Give the extent of all uninfected red blood cells.
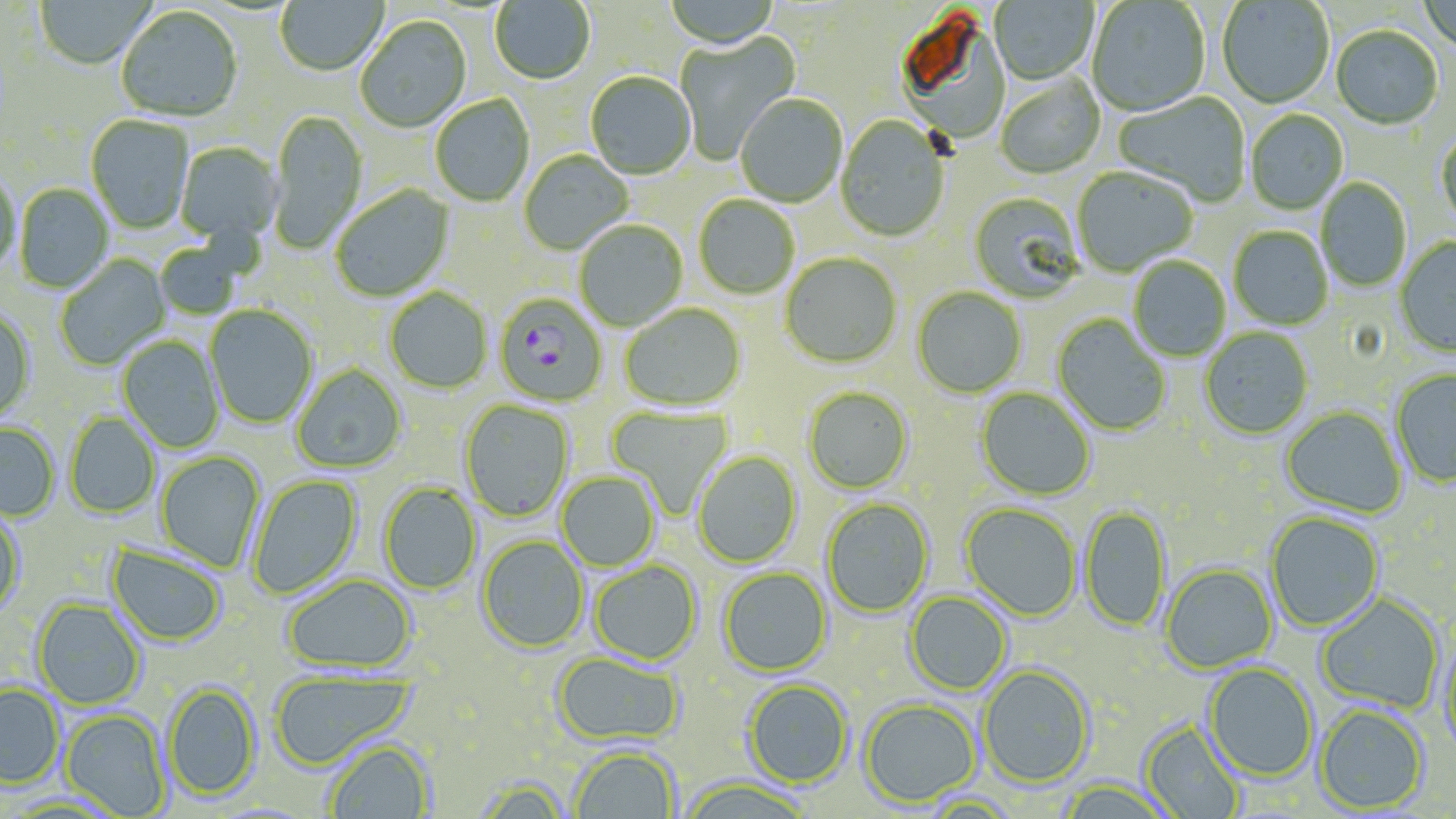
Approximate bounding boxes as (x1, y1, x2, y2) in pixels.
Uninfected red blood cells: (275, 0, 388, 78), (664, 0, 780, 51), (990, 0, 1098, 86), (1086, 0, 1210, 118), (1417, 0, 1456, 55), (34, 1, 154, 71), (490, 1, 596, 87), (1217, 1, 1334, 110), (116, 7, 243, 124), (354, 17, 472, 135), (1331, 27, 1443, 131), (674, 30, 801, 165), (585, 73, 696, 180), (996, 77, 1106, 180), (1113, 93, 1250, 207), (430, 95, 535, 207), (735, 95, 847, 208), (268, 111, 367, 256), (1245, 111, 1349, 215), (86, 115, 194, 235), (835, 117, 951, 243), (1436, 130, 1456, 232), (175, 142, 283, 242), (519, 151, 634, 256), (1071, 168, 1198, 277), (0, 171, 21, 274), (1316, 177, 1412, 293), (15, 184, 114, 294), (331, 185, 455, 302), (969, 192, 1085, 304), (694, 195, 799, 299), (573, 221, 688, 332), (1228, 226, 1333, 330), (154, 235, 254, 320), (1395, 238, 1456, 357), (780, 253, 902, 369), (54, 255, 172, 371), (1128, 256, 1231, 361), (912, 287, 1027, 398), (384, 288, 493, 394), (621, 303, 746, 411), (205, 305, 318, 429), (0, 309, 36, 421), (1052, 314, 1171, 436), (1199, 327, 1314, 440), (117, 335, 225, 454), (291, 364, 407, 474), (1390, 369, 1456, 489), (803, 386, 913, 494), (976, 388, 1096, 501), (459, 400, 574, 522), (606, 405, 735, 518), (1281, 406, 1407, 518), (65, 413, 160, 518), (0, 422, 60, 522), (156, 451, 265, 573), (693, 451, 802, 569), (556, 472, 660, 572), (248, 474, 363, 599), (379, 482, 482, 595), (820, 497, 934, 618), (960, 503, 1082, 622), (1080, 505, 1171, 634), (0, 507, 27, 616), (1265, 512, 1385, 633), (477, 536, 590, 653), (106, 542, 228, 647), (590, 559, 702, 666), (1161, 564, 1278, 673), (719, 567, 832, 677), (281, 574, 417, 674), (904, 591, 1012, 695), (1316, 593, 1445, 714), (32, 598, 145, 710), (1437, 636, 1456, 761), (552, 651, 685, 746), (1204, 662, 1318, 781), (978, 665, 1095, 788), (268, 671, 415, 770), (742, 680, 853, 788), (163, 682, 261, 800), (0, 684, 64, 788), (859, 698, 981, 807), (1315, 704, 1429, 814), (60, 709, 172, 817), (1140, 720, 1247, 819), (322, 739, 437, 818), (568, 746, 681, 819), (469, 776, 574, 819), (676, 777, 817, 819), (1055, 777, 1177, 819), (917, 793, 1025, 818).

slide_level_diagnosis: Plasmodium falciparum
stain: May-Grünwald-Giemsa
image_size: 1456×819 pixels
magnification: 1000x
plasmodium_falciparum_infected_red_blood_cell_locations: 'approximate bounding boxes as (x1, y1, x2, y2) in pixels: (495, 292, 607, 407)'
preparation: thin blood smear
modality: optical microscopy
field_of_view: one of a larger specimen